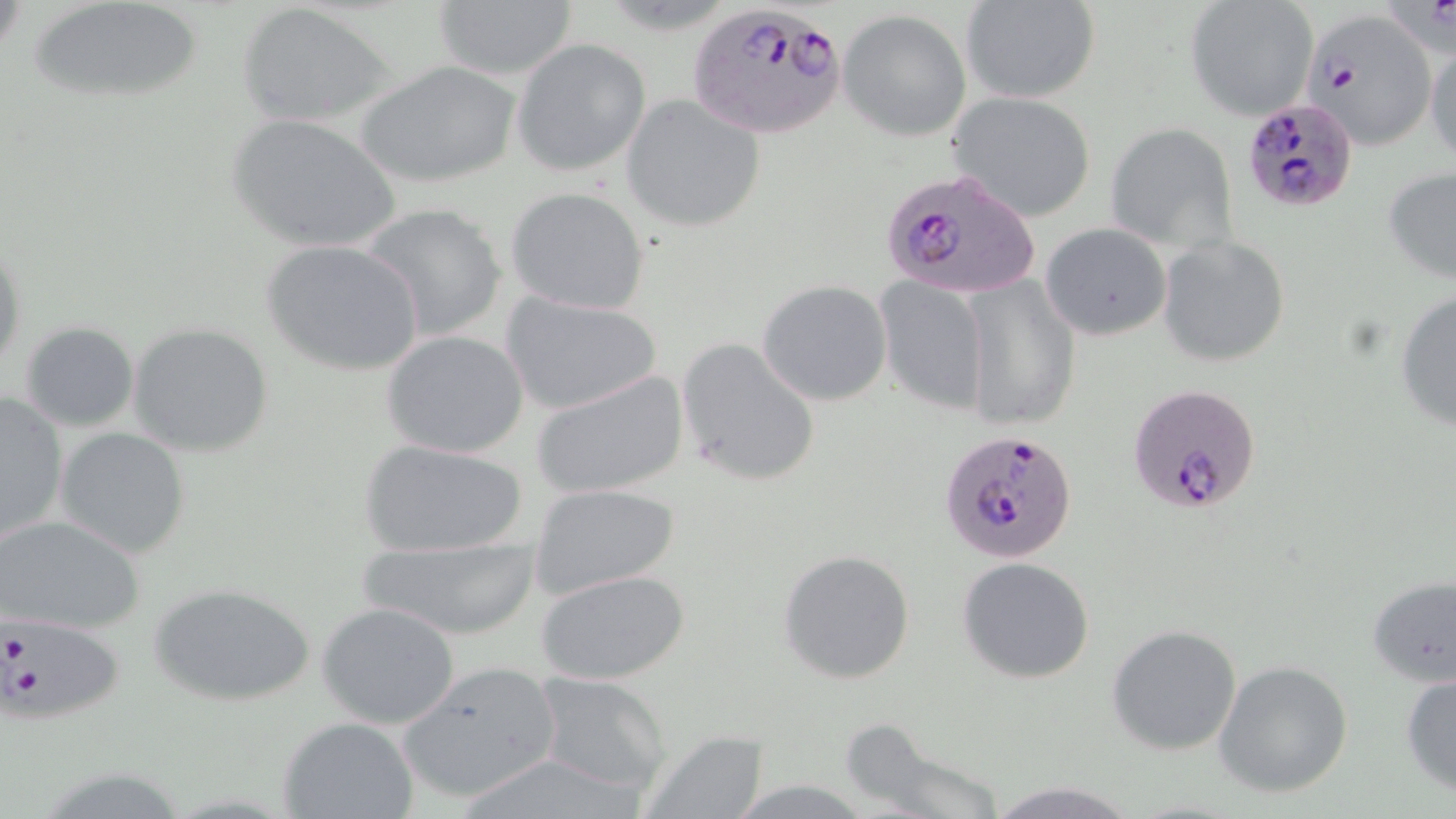
Approximate bounding boxes as (x1,y1)-(x2,y2) corner pairs in pixels. Uninfected red blood cell locations: (26,0)-(211,108), (430,0)-(579,82), (962,0)-(1101,103), (1186,1)-(1319,121), (236,4)-(394,128), (838,9)-(972,141), (1424,31)-(1456,168), (512,38)-(651,177), (354,58)-(524,189), (621,93)-(768,234), (947,93)-(1096,223), (225,114)-(404,254), (1105,122)-(1239,253), (1382,166)-(1456,286), (506,186)-(651,315), (358,202)-(510,343), (1041,222)-(1172,341), (1158,235)-(1290,367), (1,236)-(26,382), (260,238)-(425,379), (962,274)-(1080,431), (875,278)-(991,414), (757,280)-(892,406), (500,290)-(663,416), (1394,290)-(1456,434), (19,320)-(140,432), (130,322)-(273,457), (381,330)-(530,459), (676,336)-(821,488), (532,369)-(689,500), (0,392)-(69,542), (55,427)-(191,558), (357,437)-(530,559), (529,483)-(681,600), (0,514)-(146,635), (351,532)-(546,641), (778,548)-(917,684), (957,557)-(1096,683), (536,568)-(690,684), (1366,576)-(1456,688), (150,582)-(316,707), (317,601)-(462,731), (1106,624)-(1243,755), (1212,660)-(1354,798), (395,662)-(565,805), (1400,669)-(1456,800), (532,673)-(673,799), (280,717)-(420,819), (838,723)-(1013,819), (640,732)-(770,817), (984,778)-(1140,819). Plasmodium falciparum-infected red blood cell locations: (684,1)-(850,140), (1304,10)-(1439,149), (1243,100)-(1358,209), (878,166)-(1043,303), (1125,383)-(1261,514), (941,429)-(1079,563), (0,611)-(123,723). Slide-level diagnosis: Plasmodium falciparum. Image is 1456×819 pixels. May-Grünwald-Giemsa stain. Optical microscopy. Thin blood film. Single field of view. 1000x magnification.